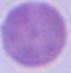
Summary:
  - Magnification: 1000x
  - Identification: erythrocyte
  - Modality: photomicrograph